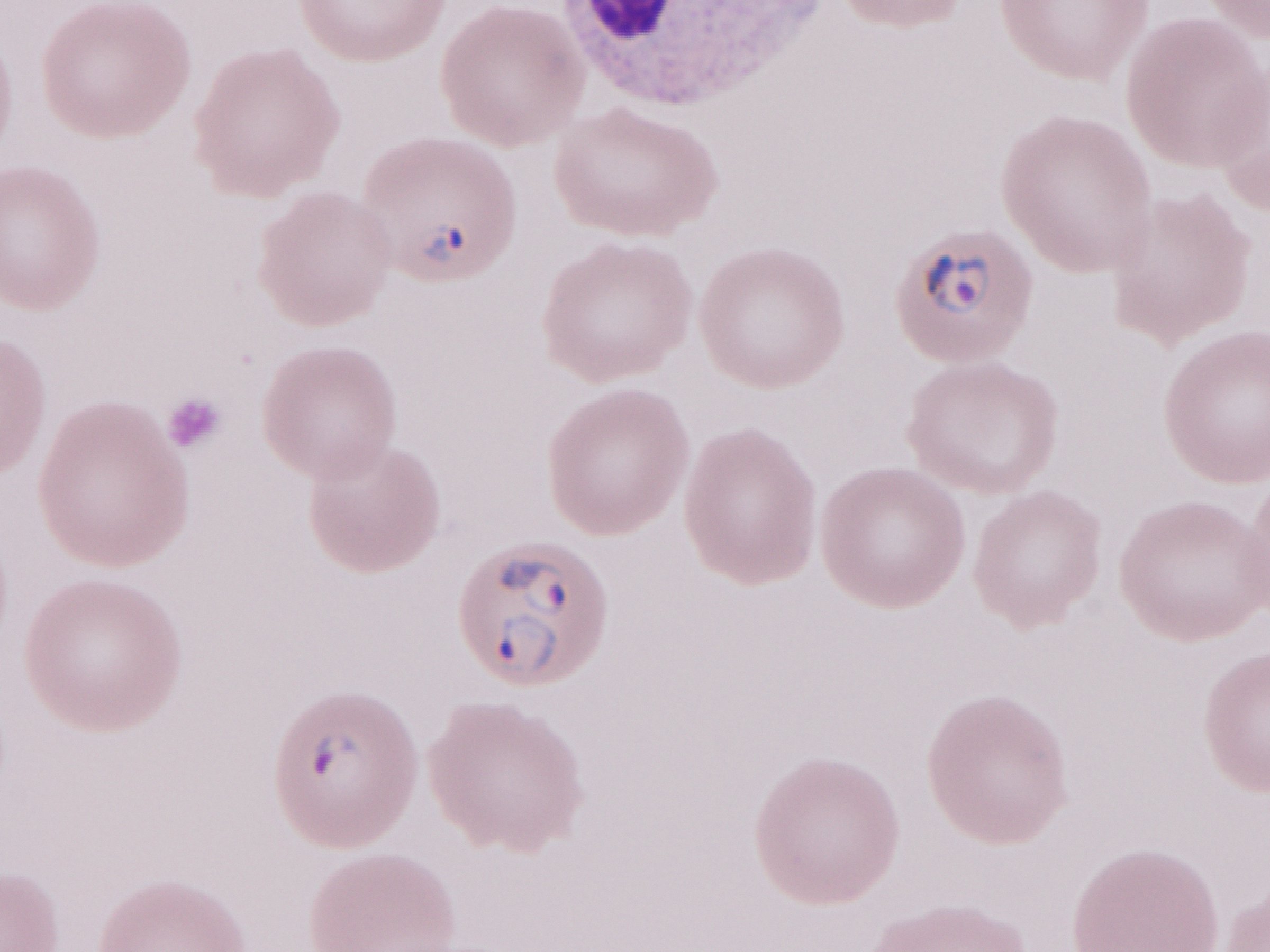

May-Grünwald-Giemsa-stained preparation. Single field of view. Patient-level malaria diagnosis: positive. Image is 1270×952 pixels. Olympus BX43 microscope and DP73 digital camera. 1,000x magnification. Thin blood film.